Classify this cell by malaria status.
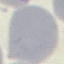
It is uninfected.

Giemsa stain. Thin blood smear. Photographed with a smartphone camera at the microscope eyepiece. Automatically extracted cell patch, resized to 64 × 64 pixels.